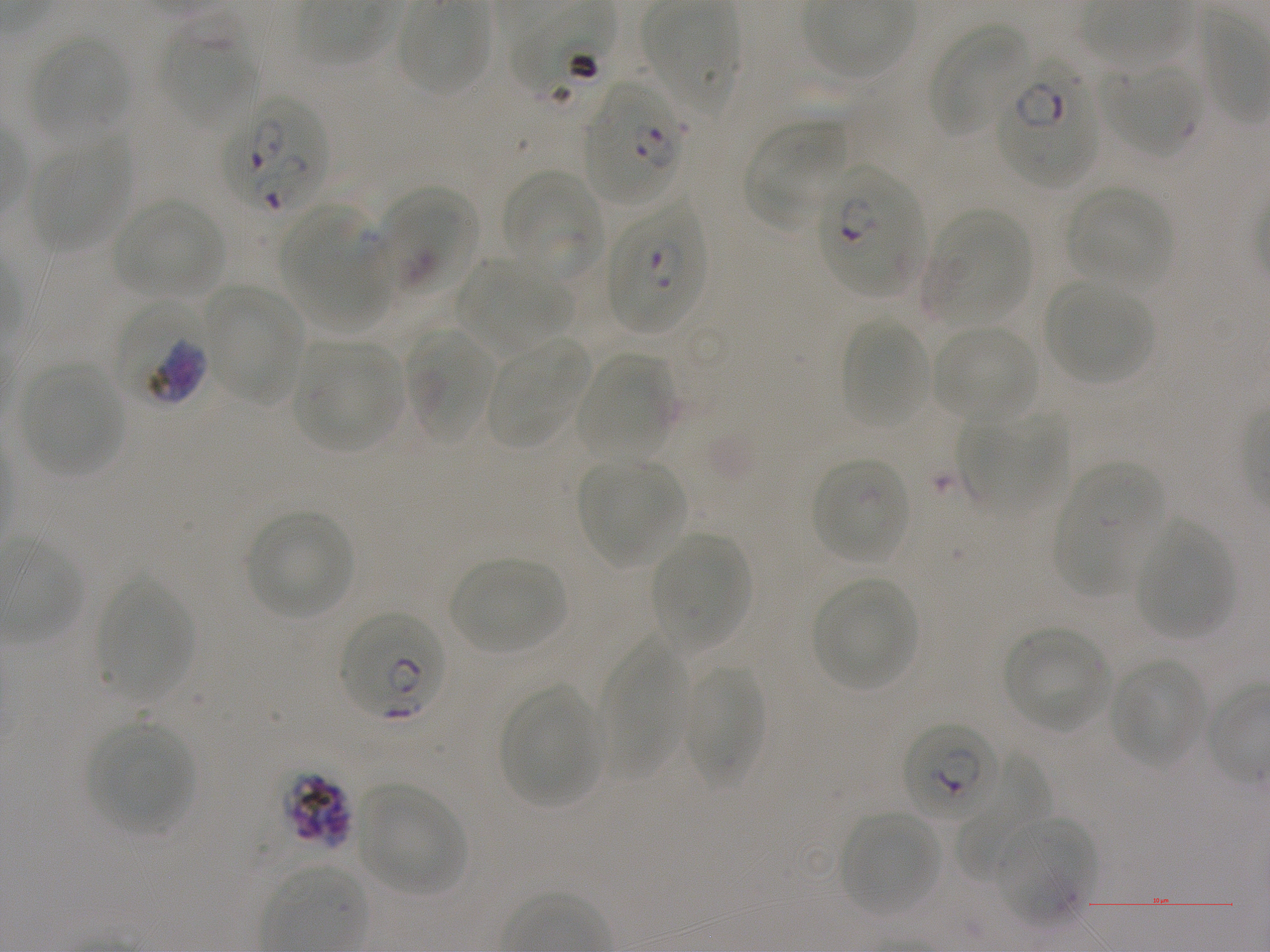 Approximate bounding boxes as [x1, y1, x2, y2] in pixels. Not every red blood cell is marked. A life-cycle stage — or a range of stages, where the recorded stages span more than one — follows each staged infected red blood cell. Locations of uninfected red blood cells: [397, 1, 490, 97], [644, 5, 741, 119], [929, 22, 1031, 136], [30, 34, 130, 138], [1100, 63, 1201, 157], [744, 120, 846, 231], [31, 136, 131, 252], [503, 171, 603, 282], [1066, 185, 1173, 291], [111, 198, 225, 299], [281, 208, 382, 324], [925, 209, 1031, 325], [456, 258, 568, 353], [1047, 281, 1151, 383], [201, 283, 304, 403], [840, 319, 929, 427], [932, 326, 1037, 424], [404, 327, 495, 445], [486, 338, 588, 450], [294, 340, 402, 452], [576, 352, 674, 460], [24, 363, 124, 476], [960, 411, 1066, 519], [577, 458, 686, 567], [811, 458, 910, 564], [1053, 463, 1165, 596], [246, 509, 354, 620], [1136, 522, 1235, 638], [651, 532, 750, 654], [449, 558, 565, 654], [813, 578, 920, 692], [97, 580, 192, 702], [1003, 626, 1112, 732], [598, 634, 686, 780], [1109, 657, 1204, 766], [682, 660, 764, 789], [501, 684, 602, 808], [87, 720, 195, 835], [957, 758, 1051, 880], [356, 782, 466, 894], [839, 811, 940, 917], [996, 817, 1093, 928]. Locations of red blood cells of indeterminate infection status: [161, 11, 257, 132], [381, 188, 477, 296]. Locations of infected red blood cells: [998, 61, 1098, 187] early ring to early trophozoite; [583, 84, 688, 204] ring; [225, 97, 329, 214]; [817, 166, 921, 296] ring; [608, 205, 707, 334]; [115, 302, 211, 407] trophozoite; [340, 611, 447, 722]; [901, 720, 999, 825] early ring to early trophozoite; [281, 769, 355, 850] schizont. Life-cycle stages observed: ring, trophozoite, schizont. Oil immersion, 100x objective (numerical aperture 1.25). Single field of view. Static in-vitro culture of P. falciparum strain NF54. Thin blood film. Blood group of the donor: A+. Image is 1270×952 pixels. Giemsa stain.